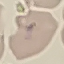
Result: no malaria parasites seen. Thin blood film. Photographed with a smartphone camera at the microscope eyepiece. Giemsa-stained preparation. Cell patch, automatically extracted from a larger field of view and resized to 64 × 64 pixels.